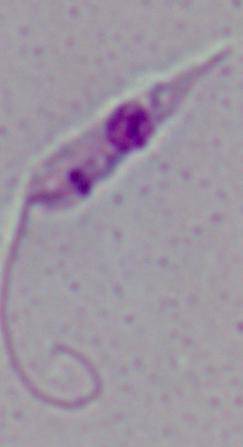

Summary:
  - Modality: photomicrograph
  - Magnification: 1000x
  - Identification: Leishmania